Comment on the morphology of the erythrocytes.
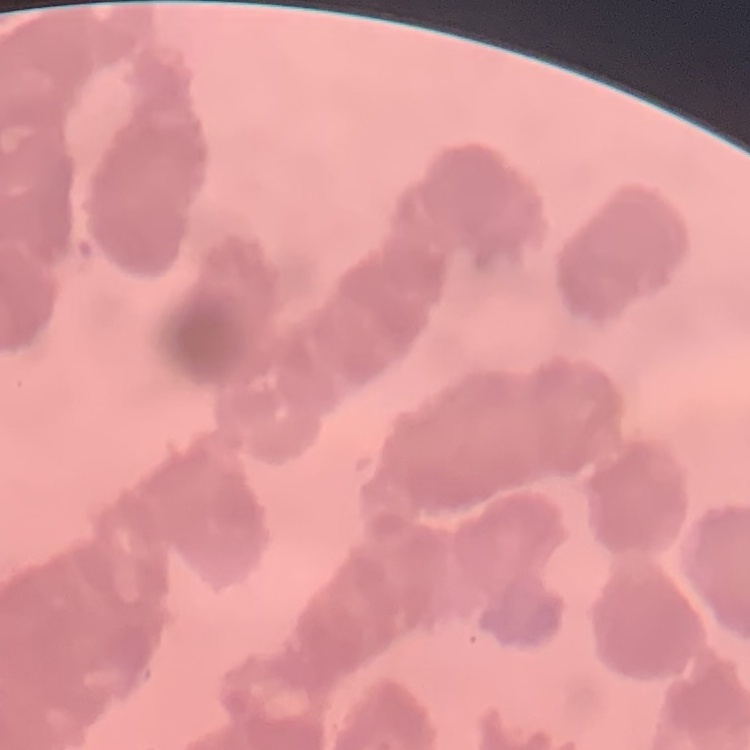
They show rouleaux formation.

Summary:
  - Stain: Field's or Giemsa
  - Image type: square crop of a larger photomicrograph
  - Preparation: thin blood film